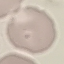
Result: no malaria parasites detected. Thin blood smear. Acquired by smartphone through the microscope eyepiece. Cell patch, automatically extracted from a larger field of view and resized to 64 × 64 pixels. Giemsa stain.